Assess this cell for malaria.
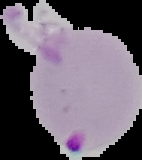
Parasitized.

Image is 142×160 pixels. From a thin blood smear. Segmented cell region on a black background.